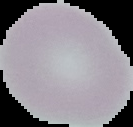
image type = segmented cell region with the area outside set to black
image size = 133×127 pixels
preparation = thin blood smear
malaria status = uninfected